Assess the morphology of the erythrocytes.
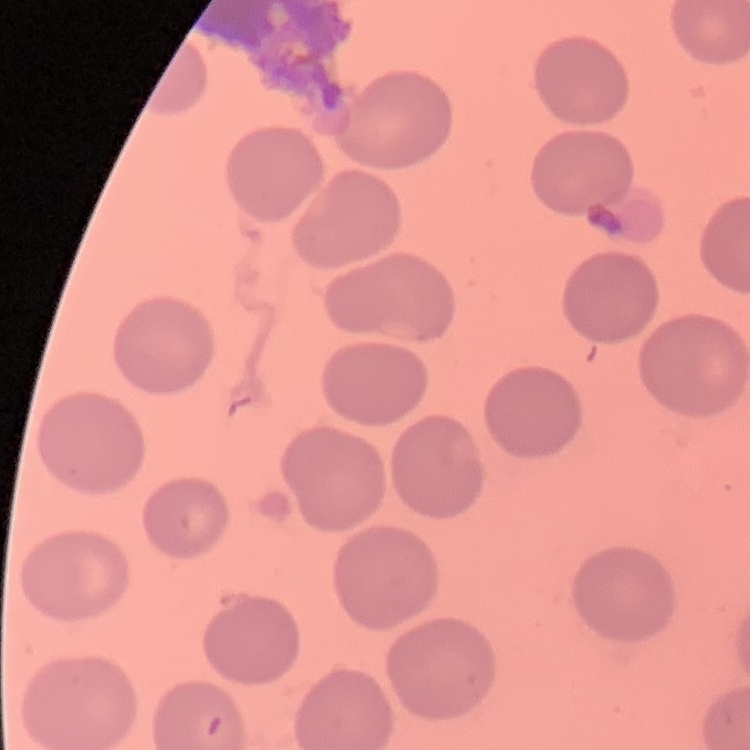
They show no rouleaux formation.

Summary:
  - Image type: one tile cut from a larger photomicrograph
  - Stain: Field's or Giemsa
  - Preparation: thin blood film